Locate every Plasmodium ovale-infected red blood cell.
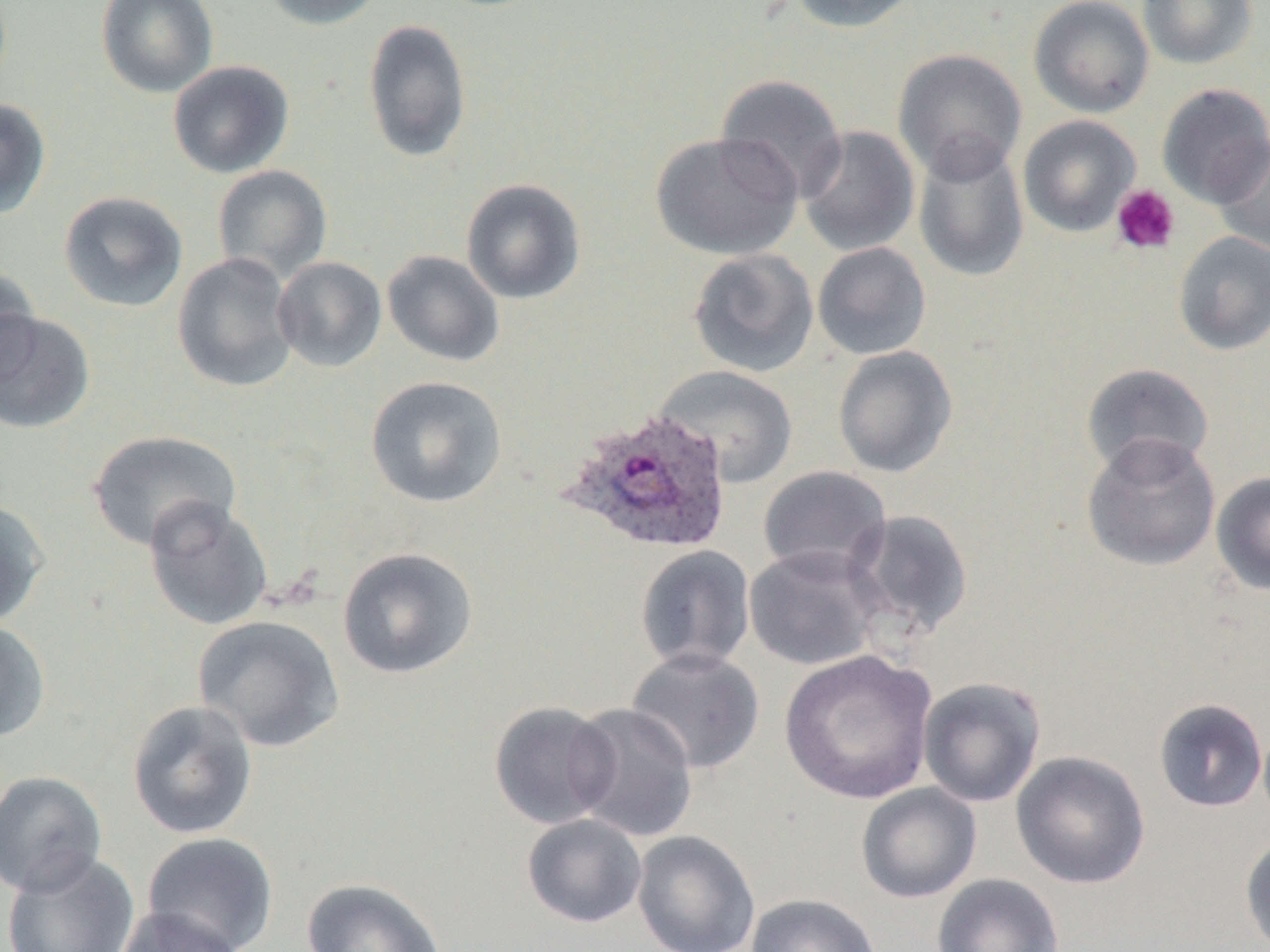
Approximate bounding boxes as [x1, y1, x2, y2] in pixels.
Plasmodium ovale-infected red blood cells: [561, 408, 735, 556].

slide-level diagnosis = Plasmodium ovale
magnification = 1000x
uninfected red blood cell locations = approximate bounding boxes as [x1, y1, x2, y2] in pixels: [96, 0, 219, 98], [258, 0, 388, 30], [785, 0, 923, 33], [1029, 0, 1155, 118], [1136, 0, 1260, 69], [362, 19, 472, 163], [892, 48, 1028, 183], [167, 60, 294, 179], [715, 74, 848, 202], [1157, 83, 1270, 208], [0, 98, 51, 219], [1017, 115, 1141, 237], [798, 125, 920, 257], [650, 131, 803, 260], [1213, 134, 1270, 256], [913, 139, 1029, 283], [212, 165, 333, 284], [460, 178, 587, 304], [58, 190, 188, 312], [1172, 231, 1270, 356], [812, 242, 931, 360], [688, 248, 819, 378], [382, 250, 505, 367], [172, 252, 298, 393], [272, 257, 387, 373], [0, 263, 41, 389], [0, 310, 95, 434], [832, 345, 958, 478], [1080, 362, 1215, 478], [654, 366, 798, 487], [365, 375, 508, 508], [86, 430, 242, 553], [1081, 433, 1222, 572], [758, 466, 892, 580], [1211, 471, 1270, 596], [142, 497, 273, 632], [0, 499, 49, 628], [847, 509, 974, 640], [634, 544, 756, 673], [744, 545, 884, 671], [337, 547, 479, 679], [193, 615, 345, 753], [0, 619, 51, 743], [625, 647, 766, 775], [779, 649, 939, 804], [918, 676, 1047, 808], [1153, 698, 1268, 813], [127, 699, 259, 840], [489, 701, 618, 830], [565, 702, 699, 842], [1011, 750, 1151, 889], [0, 770, 108, 897], [856, 783, 982, 903], [522, 813, 647, 928], [632, 830, 760, 952], [142, 831, 279, 952], [1239, 833, 1270, 952], [1, 851, 140, 952], [932, 873, 1064, 952], [300, 878, 447, 952], [745, 893, 882, 952], [111, 905, 247, 952]
modality = optical microscopy
image size = 1270×952 pixels
preparation = thin blood smear
platelet locations = approximate bounding boxes as [x1, y1, x2, y2] in pixels: [1111, 184, 1181, 255]
field of view = single